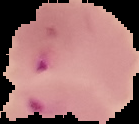
From a thin blood film. Image is 139×124 pixels. Segmented cell region on a black background. Malaria status: parasitized.